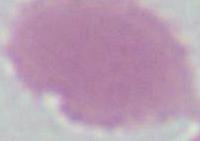
Summary:
  - Magnification: 1000x
  - Identification: erythrocyte
  - Modality: micrograph